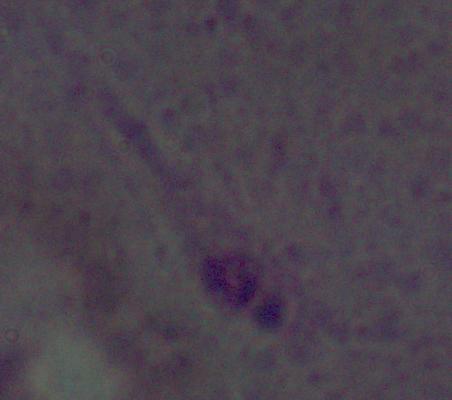
identification = Leishmania
modality = micrograph
magnification = 1000x